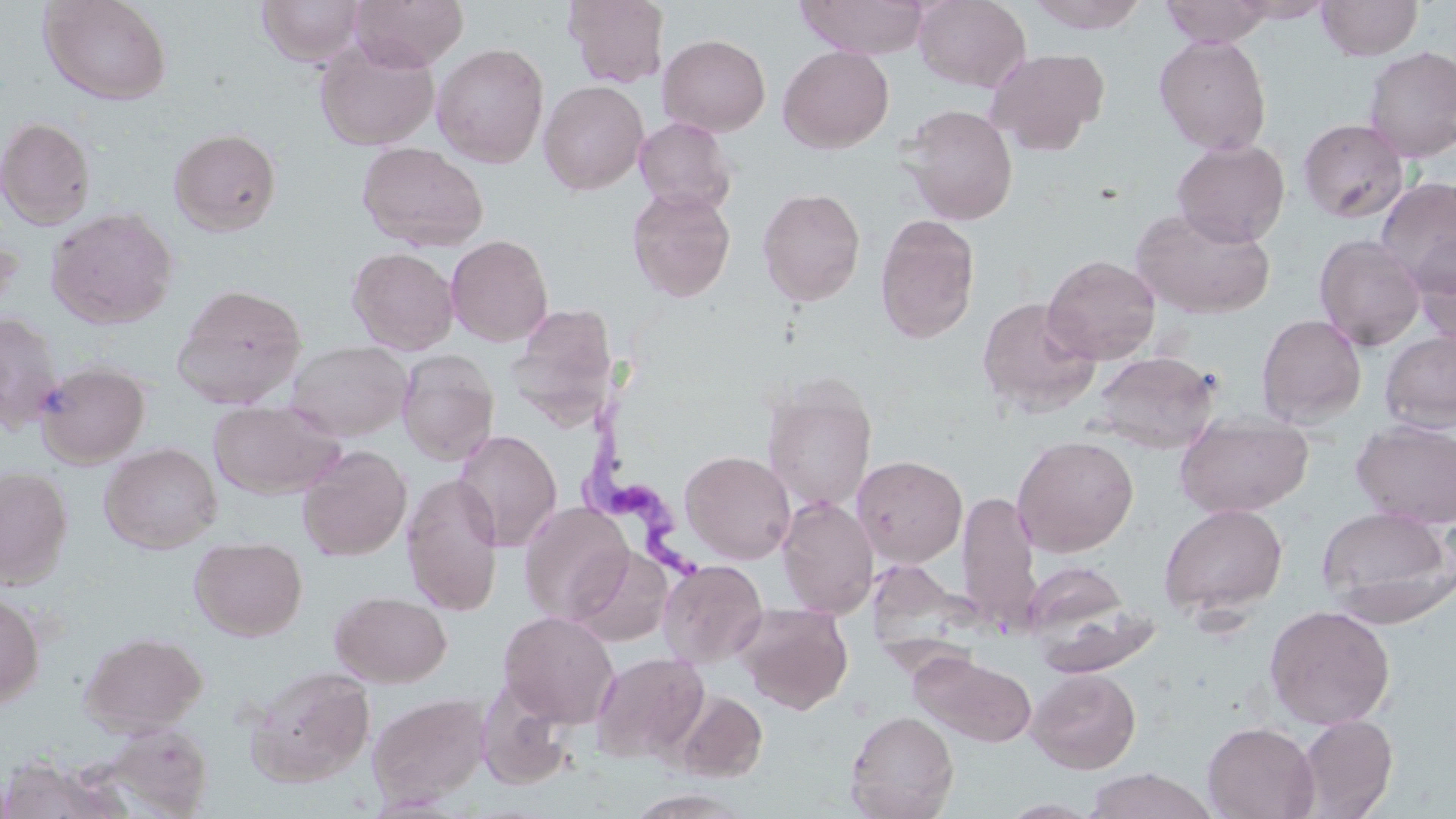 Approximate bounding boxes as (x1,y1)-(x2,y2) corner pairs in pixels. Trypanosoma brucei locations: (580,407)-(725,586). Uninfected red blood cell locations: (38,0)-(173,106), (256,0)-(367,66), (349,0)-(469,71), (563,0)-(669,88), (795,0)-(930,59), (914,0)-(1030,91), (1024,0)-(1151,33), (1158,0)-(1276,47), (1230,0)-(1335,23), (1316,0)-(1423,60), (657,34)-(771,136), (1153,34)-(1273,155), (314,37)-(440,151), (432,42)-(549,168), (778,45)-(894,153), (1361,45)-(1456,161), (984,47)-(1109,155), (538,80)-(649,195), (901,104)-(1019,226), (0,116)-(96,230), (634,116)-(738,215), (1298,118)-(1410,223), (169,128)-(282,236), (1172,139)-(1290,247), (357,141)-(488,252), (1375,176)-(1456,293), (626,186)-(736,302), (757,187)-(866,306), (46,207)-(178,329), (1131,207)-(1274,319), (875,215)-(980,344), (1410,230)-(1456,347), (446,234)-(554,347), (1314,234)-(1427,351), (347,246)-(459,355), (1042,255)-(1161,364), (171,283)-(307,409), (976,296)-(1100,417), (515,305)-(621,434), (0,312)-(64,432), (1256,313)-(1367,426), (1379,330)-(1456,434), (286,339)-(411,441), (396,350)-(499,466), (1091,350)-(1220,453), (35,362)-(151,467), (762,381)-(877,513), (208,399)-(344,499), (1174,414)-(1314,518), (1352,420)-(1456,528), (454,429)-(562,553), (1012,434)-(1139,557), (99,442)-(222,553), (297,444)-(412,561), (680,450)-(796,564), (852,455)-(967,567), (0,465)-(73,589), (401,473)-(504,616), (957,490)-(1041,633), (776,496)-(879,618), (518,502)-(635,625), (1158,503)-(1288,618), (1316,507)-(1455,622), (190,538)-(307,641), (569,546)-(674,646), (659,559)-(768,668), (1023,560)-(1129,646), (329,590)-(451,687), (0,592)-(45,710), (737,603)-(853,714), (1264,604)-(1396,730), (498,610)-(619,727), (80,631)-(207,736), (912,650)-(1038,748), (590,651)-(709,763), (245,665)-(375,787), (1028,668)-(1141,773), (474,678)-(577,790), (670,689)-(767,782), (367,692)-(491,807), (845,709)-(959,819), (1294,714)-(1398,818), (98,721)-(214,817), (1202,721)-(1320,819), (0,755)-(127,819), (1083,768)-(1217,818). Slide-level diagnosis: Trypanosoma brucei. Single field of view. 1000x magnification. May-Grünwald-Giemsa stain. Image is 1456×819 pixels. Optical microscopy. Thin blood film.